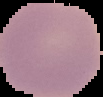
Image is 103×97 pixels. Cell region segmented out of the field of view; the surrounding area is masked to black. From a thin blood smear. Result: no malaria parasites detected.